Locate every Plasmodium parasite.
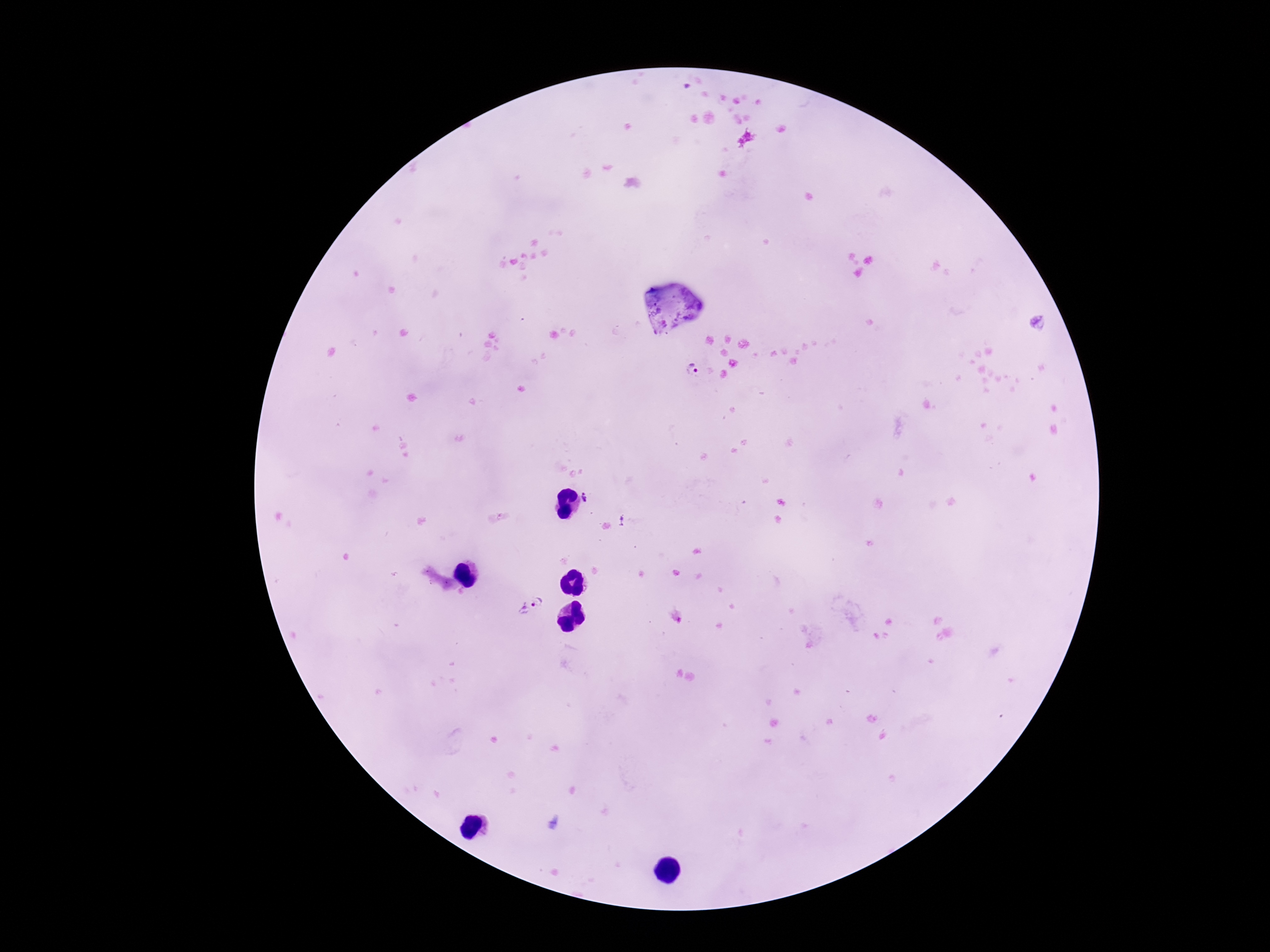

Approximate object centers, in pixels from the top-left corner.
Plasmodium parasites: (x=1038, y=322), (x=693, y=371), (x=588, y=496), (x=537, y=602).

Patient malaria status: infected. Giemsa-stained preparation. Image is 1270×952 pixels. Smartphone photograph taken through the microscope eyepiece. Single field of view. 100x magnification. Thick peripheral-blood smear.